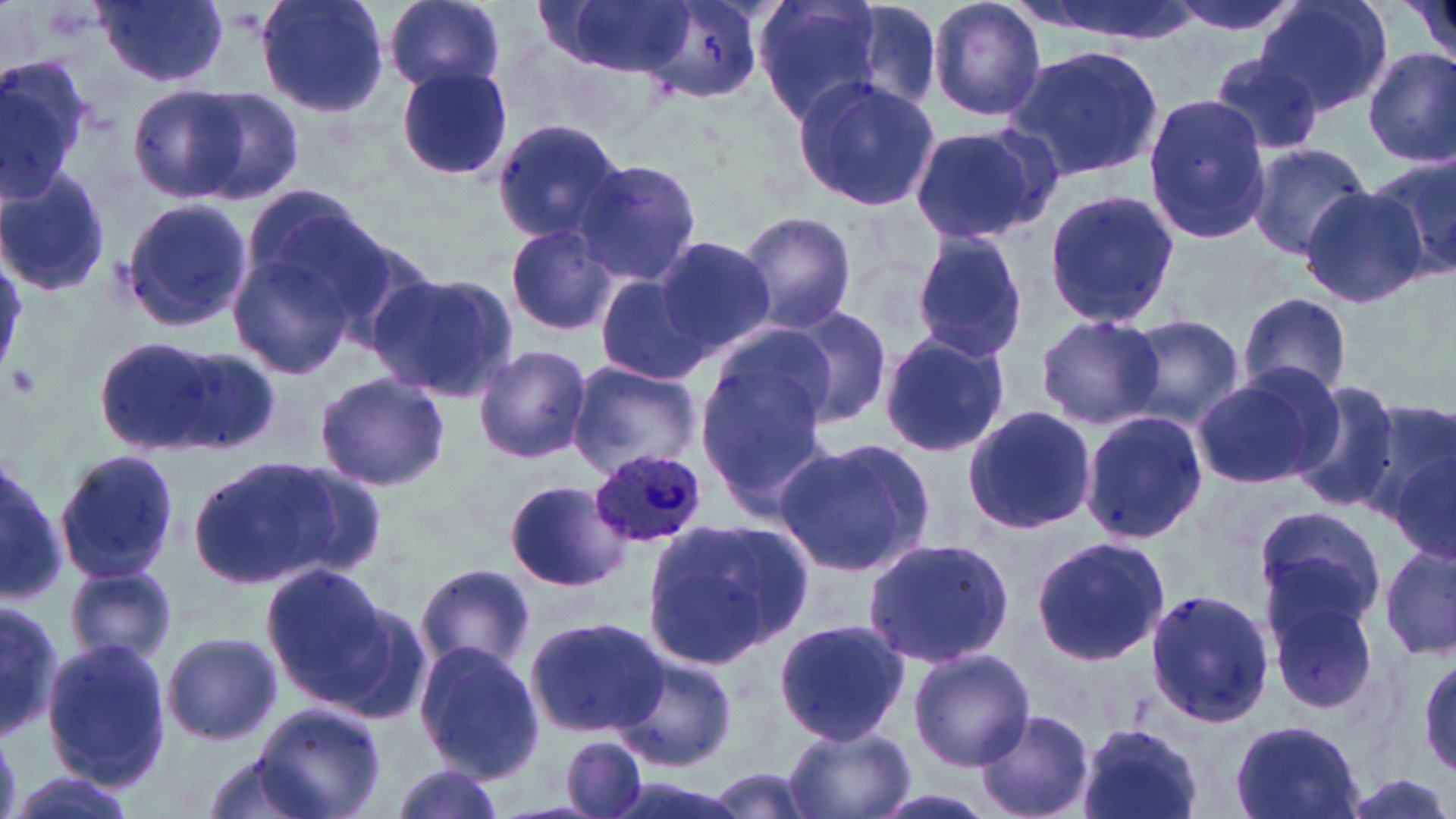

Summary:
  - Coordinate format: approximate bounding boxes as [x1, y1, x2, y2] in pixels
  - Uninfected red blood cell locations: [257, 0, 391, 118], [382, 0, 507, 94], [550, 0, 695, 76], [641, 0, 762, 103], [752, 0, 896, 128], [832, 0, 946, 119], [927, 0, 1047, 123], [1009, 0, 1199, 46], [1163, 0, 1304, 40], [1256, 0, 1391, 116], [1404, 0, 1456, 68], [95, 1, 229, 89], [1003, 46, 1164, 180], [1363, 48, 1456, 167], [1208, 53, 1323, 160], [0, 57, 95, 203], [396, 67, 513, 181], [792, 76, 940, 211], [130, 86, 248, 203], [189, 87, 306, 204], [1142, 94, 1271, 245], [491, 119, 627, 243], [907, 121, 1055, 246], [1244, 141, 1374, 259], [1370, 154, 1456, 280], [570, 159, 701, 285], [0, 168, 110, 300], [234, 182, 379, 318], [1299, 187, 1428, 308], [1042, 188, 1179, 329], [117, 197, 253, 333], [733, 210, 858, 334], [504, 222, 620, 337], [228, 230, 370, 383], [911, 232, 1029, 361], [652, 235, 774, 357], [367, 273, 519, 400], [593, 274, 712, 388], [1237, 293, 1353, 401], [784, 307, 893, 428], [1033, 313, 1165, 429], [1123, 317, 1244, 428], [878, 332, 1011, 459], [93, 336, 235, 458], [695, 340, 835, 521], [472, 345, 592, 464], [164, 347, 280, 455], [568, 362, 702, 476], [1190, 368, 1341, 490], [314, 372, 450, 493], [1287, 380, 1403, 510], [1360, 401, 1456, 533], [961, 405, 1098, 536], [1079, 410, 1208, 543], [773, 439, 933, 577], [53, 448, 180, 582], [189, 452, 385, 585], [0, 458, 71, 603], [505, 479, 631, 593], [1251, 504, 1387, 640], [646, 516, 816, 666], [860, 536, 1015, 667], [1030, 536, 1169, 665], [1380, 543, 1456, 665], [262, 561, 393, 701], [416, 563, 535, 675], [66, 565, 178, 666], [1262, 577, 1386, 718], [1144, 587, 1276, 727], [0, 593, 60, 738], [317, 601, 434, 727], [525, 615, 668, 739], [773, 619, 910, 746], [162, 631, 282, 746], [41, 637, 172, 787], [412, 642, 545, 781], [907, 647, 1036, 770], [1415, 654, 1456, 777], [615, 655, 737, 771], [253, 701, 386, 819], [971, 709, 1096, 819], [777, 720, 919, 819], [1229, 720, 1365, 819], [1074, 722, 1204, 819], [561, 735, 648, 819], [199, 754, 331, 819], [387, 761, 509, 818], [706, 767, 824, 819], [6, 773, 136, 819], [859, 784, 1011, 819]
  - Platelet locations: [8, 362, 41, 400]
  - Plasmodium ovale-infected red blood cell locations: [591, 449, 708, 547]
  - Slide-level diagnosis: Plasmodium ovale
  - Field of view: single
  - Preparation: thin blood film
  - Image size: 1456×819 pixels
  - Magnification: 1000x
  - Stain: May-Grünwald-Giemsa
  - Modality: optical microscopy